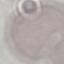

Summary:
  - Result: negative for malaria parasites
  - Stain: Giemsa
  - Capture: smartphone camera at the microscope eyepiece
  - Image type: cell patch, automatically extracted from a larger field of view and resized to 64 × 64 pixels
  - Preparation: thin blood film